Name the parasite shown.
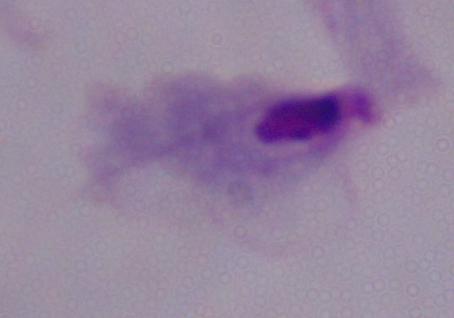
A trichomonad.

magnification = 1000x
modality = photomicrograph